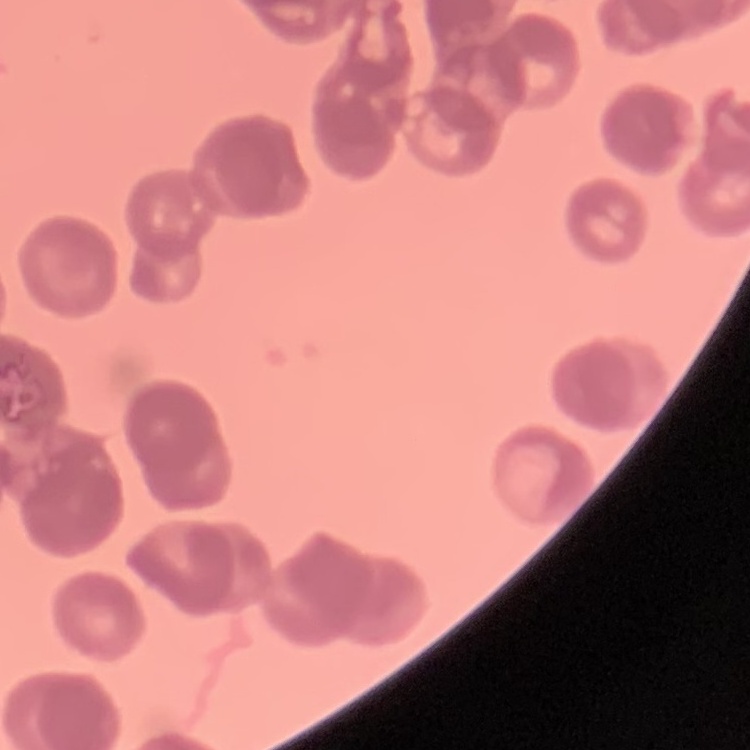

Summary:
  - Erythrocyte morphology: rouleaux formation
  - Preparation: thin blood smear
  - Image type: one tile cut from a larger photomicrograph
  - Stain: Field's or Giemsa